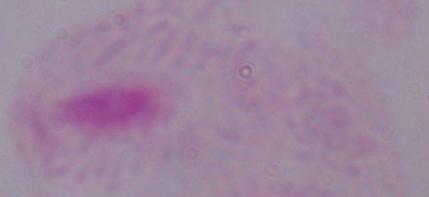
Captured at 1000x magnification. A trichomonad is shown. Photomicrograph.